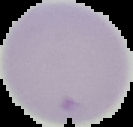
{
  "preparation": "thin blood film",
  "image_type": "cell region segmented out of the field of view; surrounding area masked to black",
  "image_size": "133×127 pixels",
  "malaria_status": "uninfected"
}